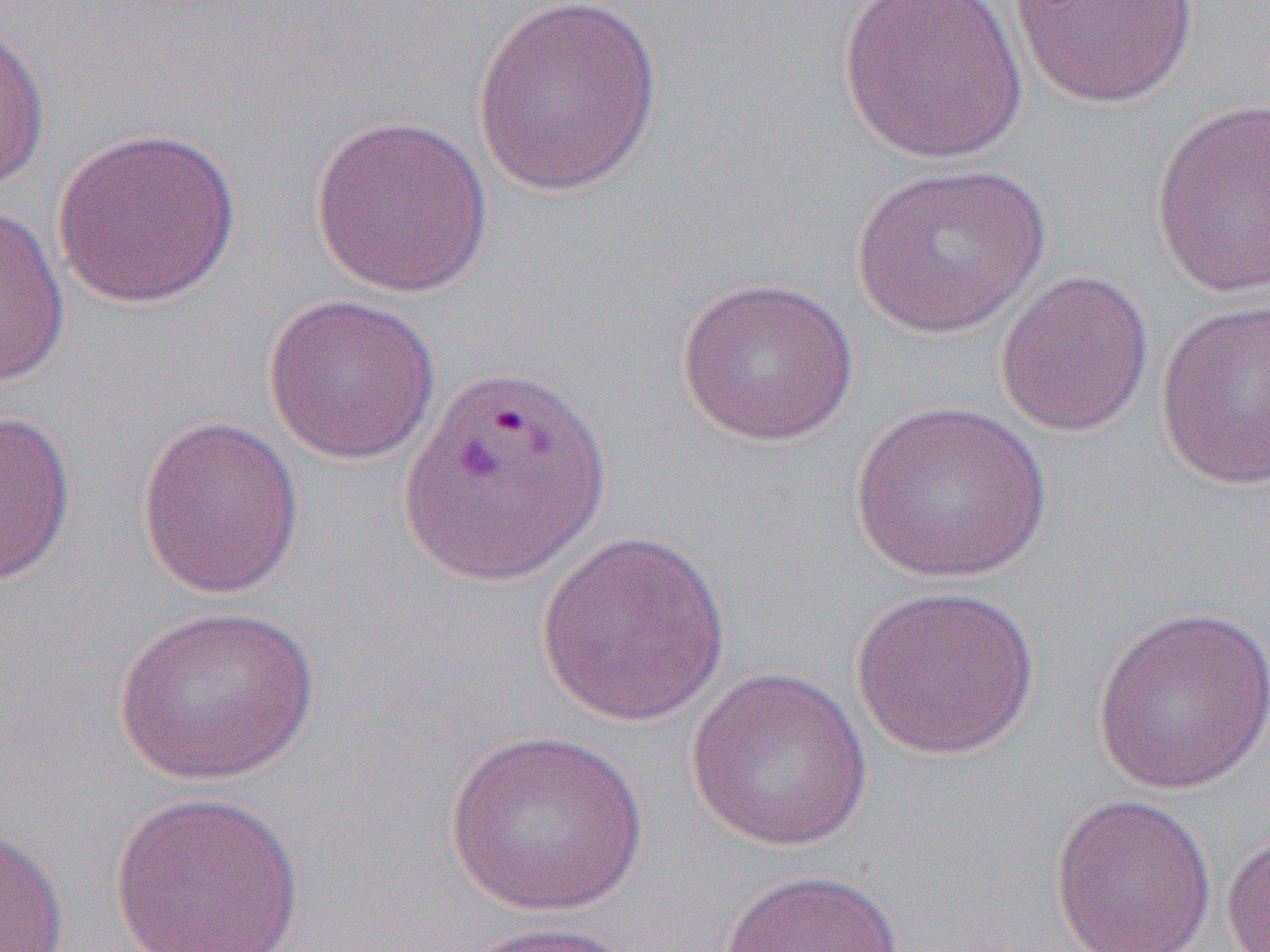
Approximate bounding boxes as [x1, y1, x2, y2] in pixels. Uninfected red blood cell locations: [470, 0, 665, 198], [836, 0, 1028, 164], [1010, 1, 1199, 109], [0, 16, 51, 193], [1150, 99, 1270, 297], [309, 113, 494, 298], [51, 125, 242, 309], [853, 164, 1050, 338], [0, 202, 70, 389], [994, 268, 1155, 438], [675, 275, 859, 446], [263, 291, 441, 464], [1155, 299, 1270, 490], [850, 398, 1053, 583], [0, 409, 77, 589], [137, 414, 305, 599], [535, 529, 733, 728], [850, 585, 1041, 760], [114, 604, 320, 785], [1092, 604, 1270, 795], [685, 665, 874, 852], [443, 728, 650, 916], [108, 789, 306, 952], [1047, 792, 1218, 952], [0, 823, 69, 951], [1220, 826, 1270, 951], [719, 867, 904, 952], [457, 919, 644, 951]. Slide-level diagnosis: Plasmodium vivax. One field of a larger specimen. Thin blood film. Captured at 1000x magnification. Image is 1270×952 pixels. Optical microscopy.